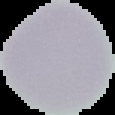
Image is 115×115 pixels. The area outside the segmented cell region is set to black. From a thin blood film. Malaria status: uninfected.